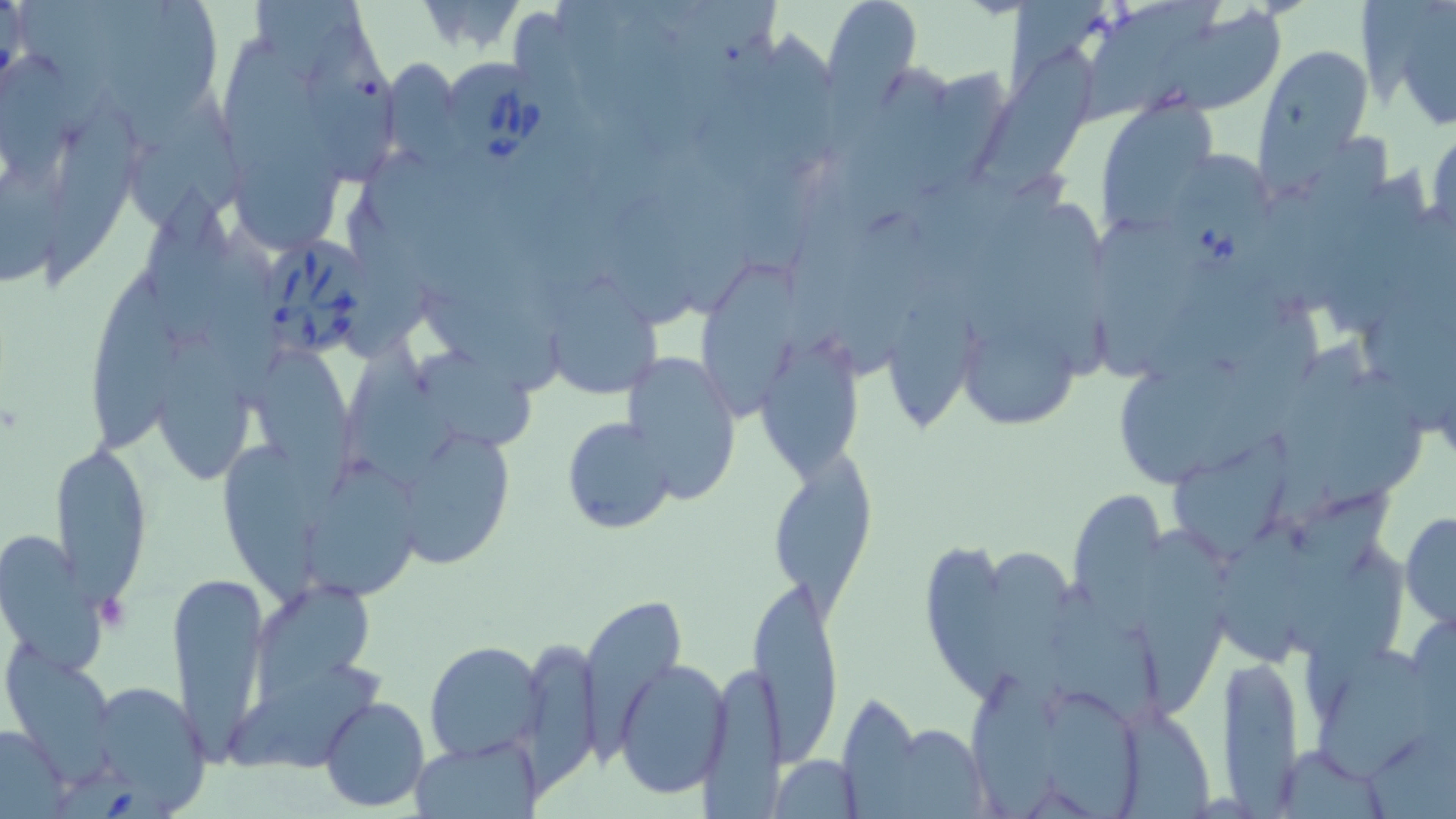

Summary:
  - Coordinate format: approximate bounding boxes as named x1/y1/x2/y2 corners in pixels
  - Uninfected red blood cell locations: (x1=822, y1=0, x2=922, y2=102), (x1=1009, y1=0, x2=1103, y2=98), (x1=1361, y1=0, x2=1456, y2=127), (x1=20, y1=1, x2=108, y2=136), (x1=255, y1=1, x2=372, y2=83), (x1=1073, y1=1, x2=1221, y2=127), (x1=606, y1=2, x2=718, y2=149), (x1=126, y1=4, x2=218, y2=143), (x1=1140, y1=10, x2=1285, y2=120), (x1=309, y1=24, x2=400, y2=196), (x1=757, y1=30, x2=852, y2=168), (x1=225, y1=37, x2=323, y2=182), (x1=973, y1=44, x2=1099, y2=201), (x1=1255, y1=46, x2=1375, y2=170), (x1=0, y1=50, x2=76, y2=183), (x1=385, y1=59, x2=461, y2=161), (x1=125, y1=92, x2=245, y2=244), (x1=1100, y1=104, x2=1212, y2=227), (x1=41, y1=108, x2=144, y2=281), (x1=1427, y1=129, x2=1455, y2=238), (x1=238, y1=159, x2=339, y2=256), (x1=0, y1=163, x2=69, y2=288), (x1=1320, y1=167, x2=1430, y2=344), (x1=143, y1=178, x2=242, y2=353), (x1=341, y1=193, x2=439, y2=361), (x1=1017, y1=199, x2=1109, y2=394), (x1=199, y1=215, x2=288, y2=394), (x1=1097, y1=219, x2=1205, y2=378), (x1=699, y1=258, x2=813, y2=422), (x1=86, y1=271, x2=186, y2=459), (x1=550, y1=275, x2=665, y2=399), (x1=887, y1=276, x2=969, y2=440), (x1=417, y1=285, x2=563, y2=398), (x1=1196, y1=314, x2=1324, y2=472), (x1=970, y1=327, x2=1081, y2=433), (x1=155, y1=329, x2=258, y2=488), (x1=341, y1=330, x2=454, y2=494), (x1=1273, y1=333, x2=1377, y2=514), (x1=765, y1=342, x2=858, y2=492), (x1=259, y1=350, x2=355, y2=526), (x1=413, y1=351, x2=536, y2=453), (x1=620, y1=352, x2=740, y2=507), (x1=1120, y1=364, x2=1250, y2=481), (x1=1325, y1=368, x2=1429, y2=519), (x1=559, y1=416, x2=676, y2=537), (x1=405, y1=433, x2=514, y2=574), (x1=1171, y1=433, x2=1293, y2=558), (x1=48, y1=439, x2=155, y2=612), (x1=225, y1=439, x2=317, y2=615), (x1=765, y1=447, x2=880, y2=612), (x1=304, y1=452, x2=426, y2=602), (x1=1289, y1=487, x2=1392, y2=647), (x1=1068, y1=488, x2=1170, y2=616), (x1=1400, y1=510, x2=1456, y2=627), (x1=1206, y1=520, x2=1319, y2=681), (x1=0, y1=527, x2=110, y2=675), (x1=1140, y1=530, x2=1231, y2=719), (x1=991, y1=543, x2=1074, y2=716), (x1=1309, y1=545, x2=1406, y2=716), (x1=924, y1=546, x2=1040, y2=717), (x1=165, y1=573, x2=272, y2=761), (x1=746, y1=573, x2=844, y2=763), (x1=248, y1=579, x2=375, y2=709), (x1=1044, y1=579, x2=1168, y2=725), (x1=582, y1=596, x2=687, y2=745), (x1=425, y1=641, x2=546, y2=762), (x1=1310, y1=644, x2=1440, y2=781), (x1=517, y1=646, x2=601, y2=794), (x1=5, y1=649, x2=117, y2=776), (x1=1217, y1=653, x2=1306, y2=805), (x1=614, y1=658, x2=731, y2=799), (x1=700, y1=662, x2=785, y2=819), (x1=219, y1=663, x2=387, y2=767), (x1=965, y1=667, x2=1056, y2=819), (x1=78, y1=680, x2=212, y2=814), (x1=1048, y1=689, x2=1146, y2=819), (x1=836, y1=690, x2=924, y2=809), (x1=320, y1=695, x2=430, y2=810), (x1=1120, y1=708, x2=1213, y2=819), (x1=876, y1=720, x2=989, y2=816), (x1=0, y1=724, x2=71, y2=814), (x1=414, y1=737, x2=539, y2=816), (x1=1269, y1=744, x2=1388, y2=817), (x1=769, y1=753, x2=864, y2=818)
  - Platelet locations: (x1=96, y1=593, x2=132, y2=634)
  - Babesia divergens-infected red blood cell locations: (x1=439, y1=62, x2=558, y2=178), (x1=1169, y1=144, x2=1283, y2=272), (x1=262, y1=240, x2=377, y2=357), (x1=58, y1=766, x2=178, y2=819)
  - Slide-level diagnosis: Babesia divergens
  - Stain: May-Grünwald-Giemsa
  - Field of view: single
  - Image size: 1456×819 pixels
  - Preparation: thin blood film
  - Magnification: 1000x
  - Modality: light microscopy